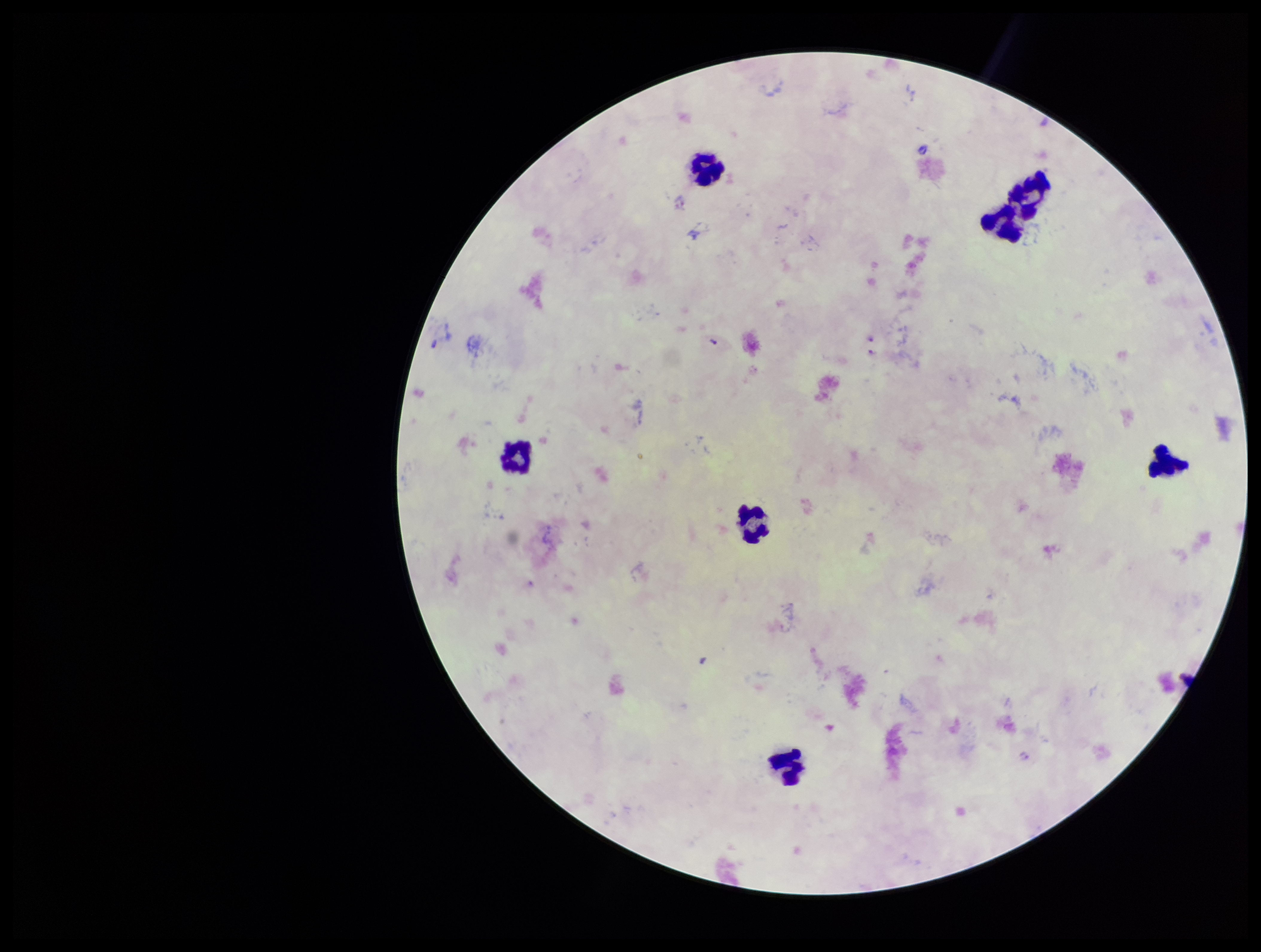

{
  "preparation": "thick blood smear",
  "image_size": "1261×952 pixels",
  "capture": "smartphone photograph through the microscope eyepiece",
  "field_of_view": "one from this slide",
  "parasite_count": 6,
  "leukocyte_count": 7,
  "patient_malaria_status": "infected",
  "plasmodium_parasites": "detected",
  "stain": "Giemsa",
  "species_reported_for_this_patient": "Plasmodium falciparum"
}